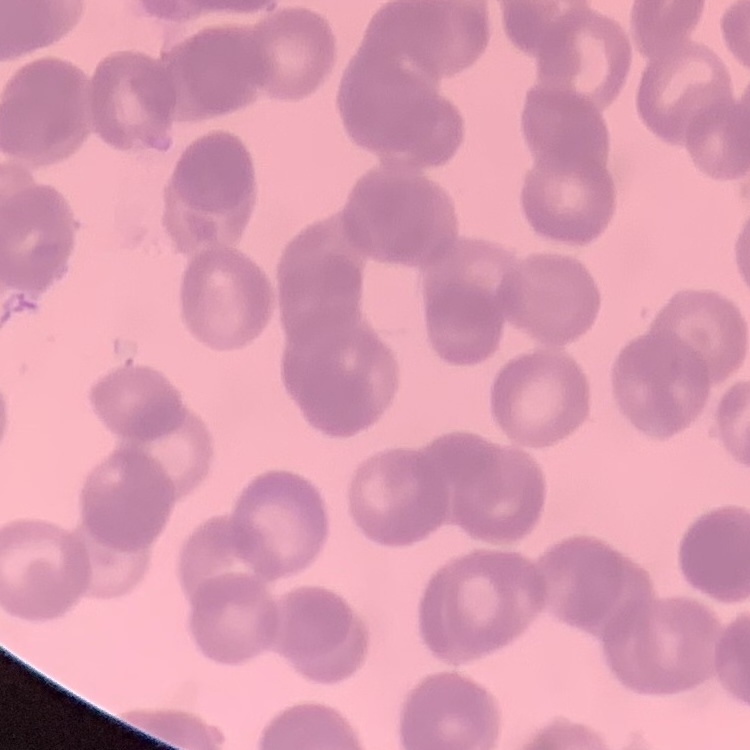
erythrocyte morphology = rouleaux formation
image type = square crop of a larger photomicrograph
preparation = thin peripheral smear
stain = Field's or Giemsa